Assess this cell for malaria.
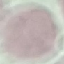
Uninfected.

image type = automatically extracted cell patch, resized to 64 × 64 pixels
preparation = thin blood film
stain = Giemsa
capture = smartphone through the microscope eyepiece